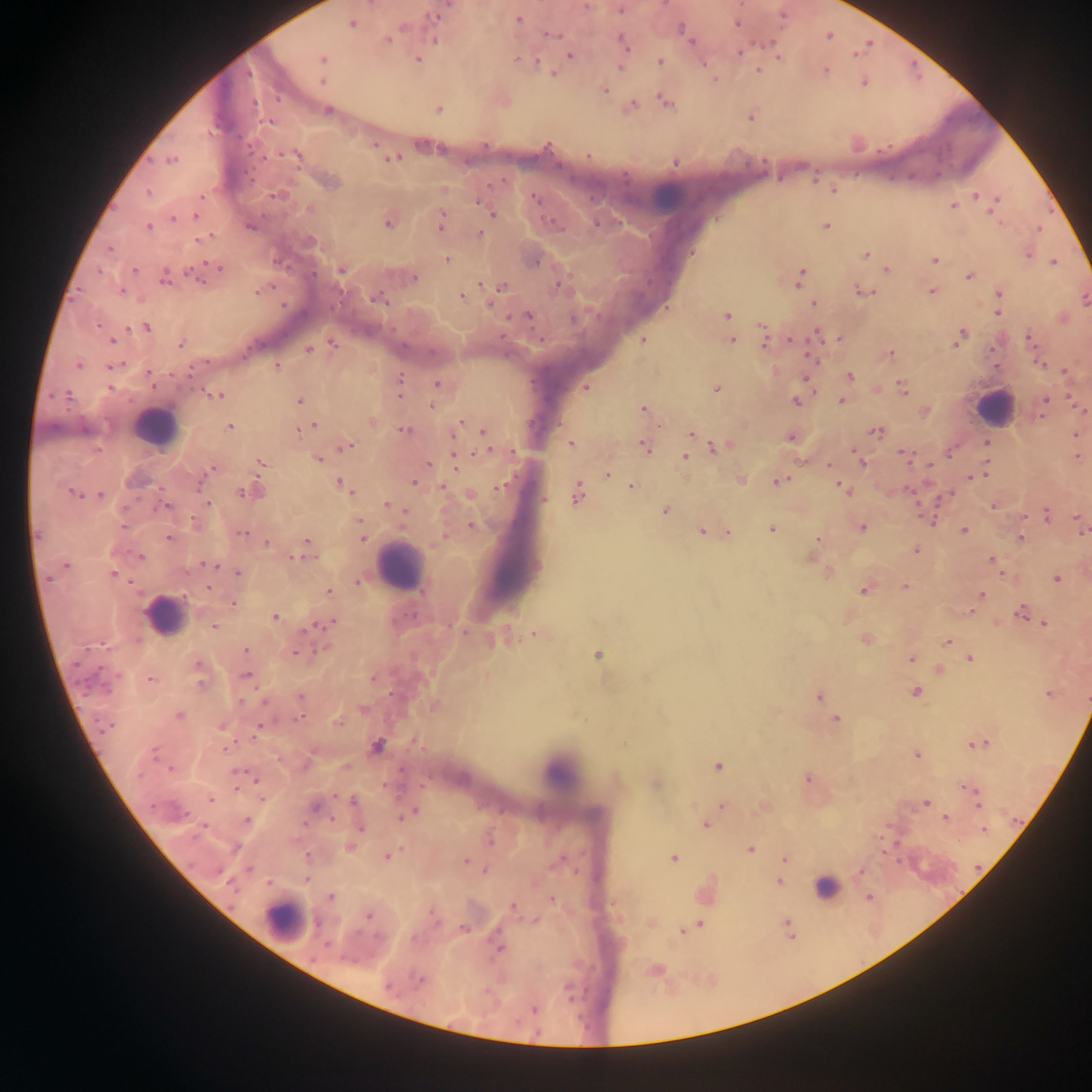
Approximate centers as [x, y] in pixels. Plasmodium parasite locations: [586, 6], [621, 9], [435, 16], [519, 20], [351, 24], [403, 27], [682, 29], [552, 35], [829, 35], [435, 39], [387, 40], [691, 40], [623, 42], [740, 52], [855, 54], [570, 55], [778, 57], [322, 59], [417, 60], [516, 60], [660, 61], [537, 62], [620, 66], [758, 70], [826, 70], [322, 81], [863, 82], [605, 90], [665, 102], [632, 106], [328, 110], [438, 110], [751, 117], [269, 123], [297, 155], [588, 155], [394, 159], [171, 160], [676, 163], [331, 182], [834, 190], [148, 192], [276, 196], [976, 196], [201, 197], [536, 198], [998, 198], [479, 203], [953, 206], [310, 209], [992, 211], [492, 214], [196, 217], [173, 219], [441, 222], [387, 223], [597, 224], [826, 225], [148, 226], [250, 226], [1038, 229], [480, 234], [201, 239], [310, 242], [109, 250], [865, 254], [1028, 255], [446, 260], [934, 260], [1054, 262], [536, 263], [219, 268], [341, 270], [886, 270], [135, 271], [99, 272], [969, 276], [414, 278], [801, 278], [164, 279], [198, 279], [481, 284], [559, 284], [502, 286], [122, 292], [258, 292], [864, 292], [932, 292], [999, 294], [461, 295], [378, 299], [490, 303], [815, 303], [998, 313], [528, 316], [727, 316], [573, 319], [128, 327], [148, 327], [762, 327], [817, 334], [838, 338], [961, 338], [1029, 338], [732, 340], [112, 341], [643, 341], [793, 341], [180, 344], [333, 344], [764, 344], [307, 349], [890, 353], [813, 358], [1039, 363], [78, 366], [112, 366], [276, 366], [190, 372], [1065, 372], [149, 374], [850, 376], [400, 379], [806, 379], [437, 383], [903, 387], [110, 388], [585, 388], [715, 389], [217, 396], [299, 400], [1044, 400], [796, 401], [842, 401], [432, 406], [643, 409], [926, 412], [371, 421], [459, 424], [313, 425], [230, 427], [85, 429], [299, 430], [405, 430], [484, 431], [877, 431], [692, 433], [1075, 434], [790, 437], [571, 443], [986, 443], [347, 446], [687, 446], [644, 447], [717, 447], [856, 453], [905, 455], [684, 456], [1077, 458], [318, 459], [456, 460], [861, 460], [261, 463], [428, 463], [930, 464], [829, 465], [212, 469], [607, 474], [974, 477], [741, 480], [779, 481], [413, 482], [200, 484], [342, 484], [631, 486], [347, 487], [442, 487], [500, 487], [843, 488], [72, 492], [244, 492], [576, 493], [100, 495], [207, 504], [387, 505], [993, 505], [165, 506], [665, 511], [405, 513], [1047, 516], [359, 520], [930, 520], [195, 523], [1078, 523], [124, 526], [470, 526], [862, 528], [772, 530], [1082, 530], [701, 531], [964, 531], [728, 532], [242, 533], [38, 535], [168, 538], [362, 539], [1021, 539], [817, 540], [306, 541], [266, 544], [915, 550], [140, 557], [298, 558], [992, 560], [67, 565], [209, 565], [237, 572], [113, 575], [48, 578], [1056, 579], [358, 581], [905, 587], [208, 588], [864, 590], [329, 592], [982, 595], [233, 604], [1021, 611], [275, 616], [328, 623], [1045, 624], [215, 627], [536, 634], [866, 639], [947, 641], [246, 649], [296, 654], [597, 655], [970, 658], [911, 659], [198, 665], [246, 675], [373, 679], [150, 680], [201, 683], [916, 692], [1050, 694], [300, 697], [819, 697], [241, 702], [435, 706], [363, 709], [179, 715], [299, 718], [836, 719], [337, 723], [222, 726], [108, 727], [256, 731], [981, 743], [377, 745], [226, 748], [154, 754], [917, 755], [345, 766], [718, 766], [169, 769], [239, 773], [808, 779], [655, 783], [972, 788], [261, 797], [210, 799], [353, 801], [926, 802], [978, 804], [721, 805], [315, 807], [410, 813], [946, 818], [246, 820], [705, 826], [360, 829], [984, 830], [350, 848], [750, 849], [388, 856], [673, 858], [785, 858], [466, 860], [249, 868], [485, 871], [861, 872], [307, 879], [779, 881], [229, 883], [331, 897], [869, 898], [552, 899], [512, 907], [368, 916], [535, 921], [787, 922], [700, 924], [464, 928], [682, 932], [500, 948], [419, 981], [389, 988], [534, 1010]. Leukocyte locations: [667, 197], [993, 408], [155, 427], [400, 567], [165, 614], [559, 771], [825, 885], [283, 920]. Photographed through a microscope with a mobile-phone camera. Sample from Ghana. One field of view. Thick blood film. Image is 1092×1092 pixels.